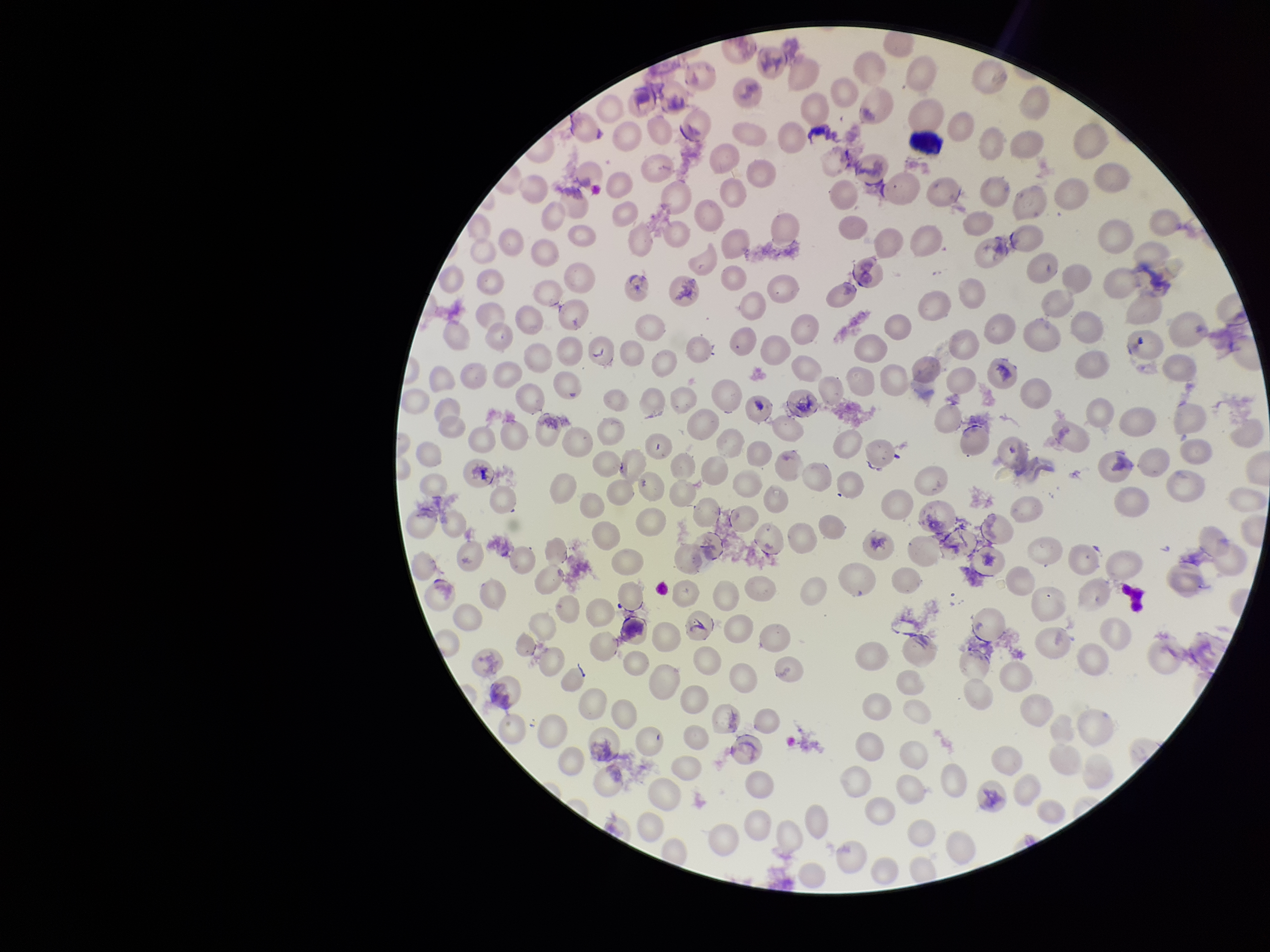
Summary:
  - Red blood cell count: 238
  - Patient malaria status: infected
  - Image size: 1270×952 pixels
  - Capture: smartphone photograph through the microscope eyepiece
  - Parasitized red blood cells: detected
  - Stain: Giemsa
  - Field of view: single
  - Preparation: thin
  - Species reported for this patient: Plasmodium vivax
  - Parasitized red blood cell count: 1